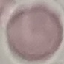
Malaria status: uninfected. Photographed with a smartphone camera at the microscope eyepiece. Automatically extracted cell patch, resized to 64 × 64 pixels. Giemsa-stained preparation. Thin smear of blood.